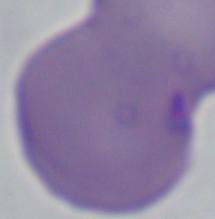
identification = Babesia
magnification = 1000x
modality = photomicrograph